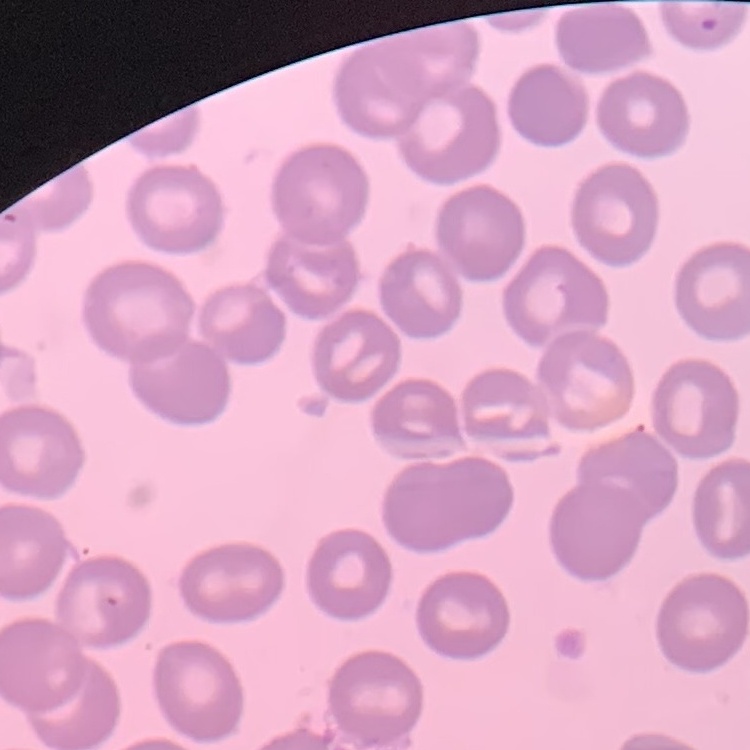
Summary:
  - Erythrocyte morphology: no rouleaux formation
  - Image type: one tile cut from a larger photomicrograph
  - Preparation: thin peripheral smear
  - Stain: Field's or Giemsa